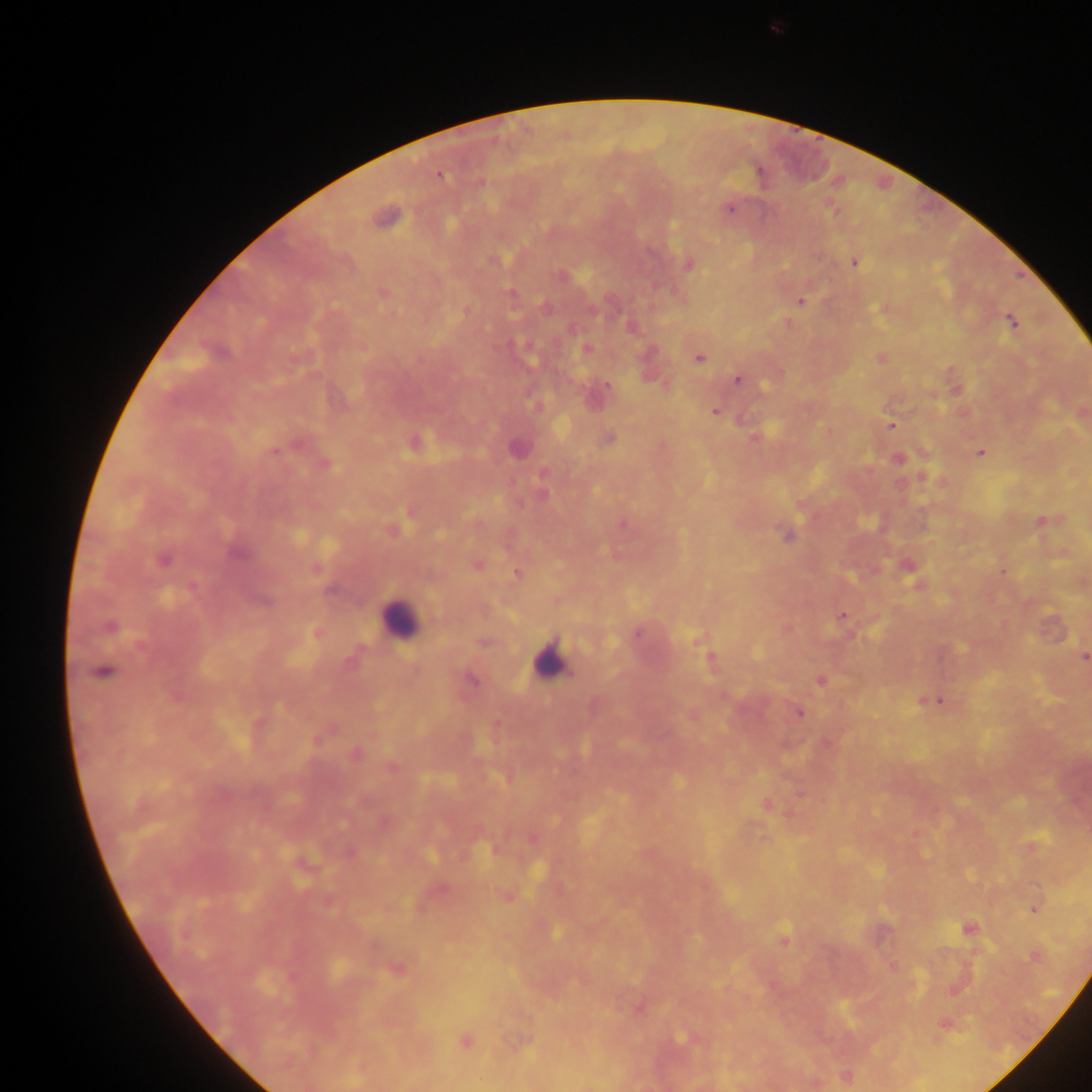

Approximate centers as {x, y} in pixels. Malaria parasite locations: {759, 171}, {440, 176}, {480, 183}, {729, 209}, {834, 210}, {855, 262}, {688, 266}, {383, 292}, {511, 294}, {800, 301}, {1012, 321}, {586, 349}, {699, 358}, {737, 380}, {608, 384}, {714, 411}, {891, 425}, {609, 438}, {518, 449}, {274, 451}, {980, 453}, {899, 459}, {326, 464}, {543, 494}, {1042, 521}, {623, 525}, {786, 535}, {236, 553}, {162, 560}, {477, 565}, {516, 574}, {192, 588}, {842, 615}, {110, 627}, {637, 633}, {483, 643}, {1084, 657}, {711, 658}, {104, 672}, {821, 680}, {472, 681}, {939, 701}, {799, 713}, {355, 754}, {392, 768}, {767, 805}, {350, 853}, {1034, 909}, {968, 928}, {556, 932}, {783, 941}, {1035, 957}, {396, 970}, {638, 1009}, {944, 1025}, {682, 1038}, {465, 1040}. Leukocyte locations: {400, 618}, {547, 661}. One field of view. Image is 1092×1092 pixels. Mobile-phone photograph taken through the microscope. Sample from Ghana. Thick blood film.